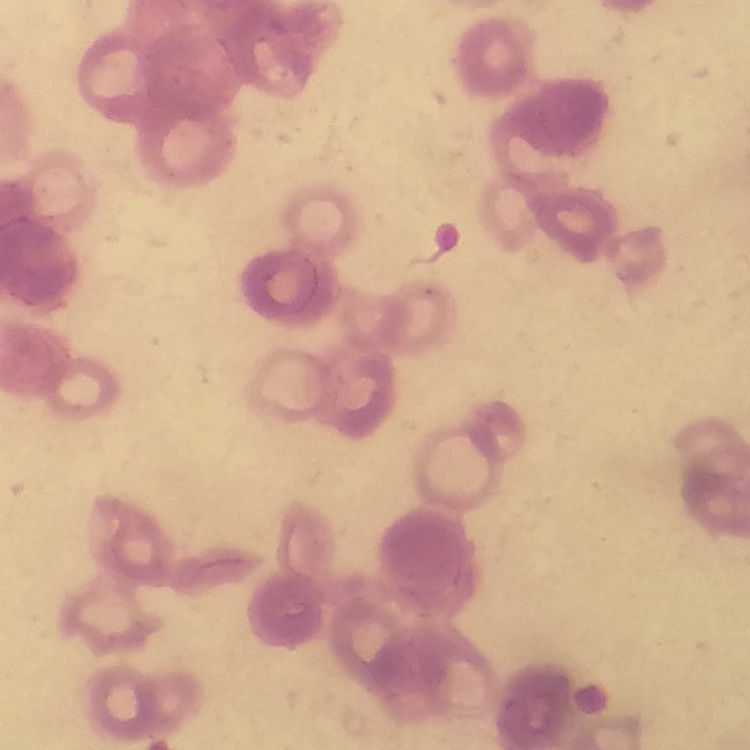
Summary:
  - Erythrocyte morphology: rouleaux formation
  - Preparation: thin blood smear
  - Image type: square crop of a larger photomicrograph
  - Stain: Field's or Giemsa